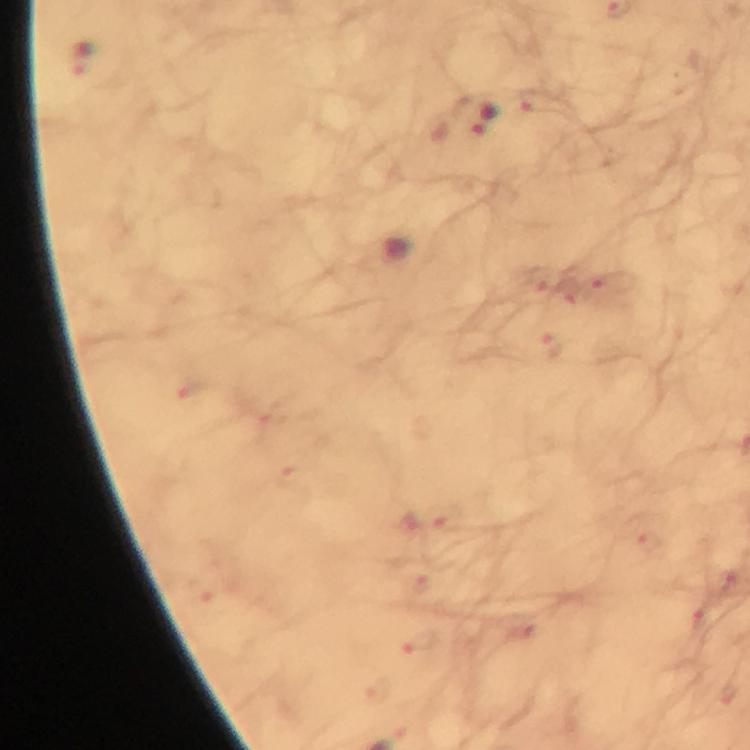 Approximate centers as [x, y] in pixels. Malaria parasite locations: [82, 58], [475, 116]. Image is 750×750 pixels. A crop from one field of view. From a diagnostic examination for malaria. Giemsa-stained preparation. Immersion oil applied. Smartphone photograph taken through a microscope. 100x magnification. Thick blood film.